Identify the blood parasite species.
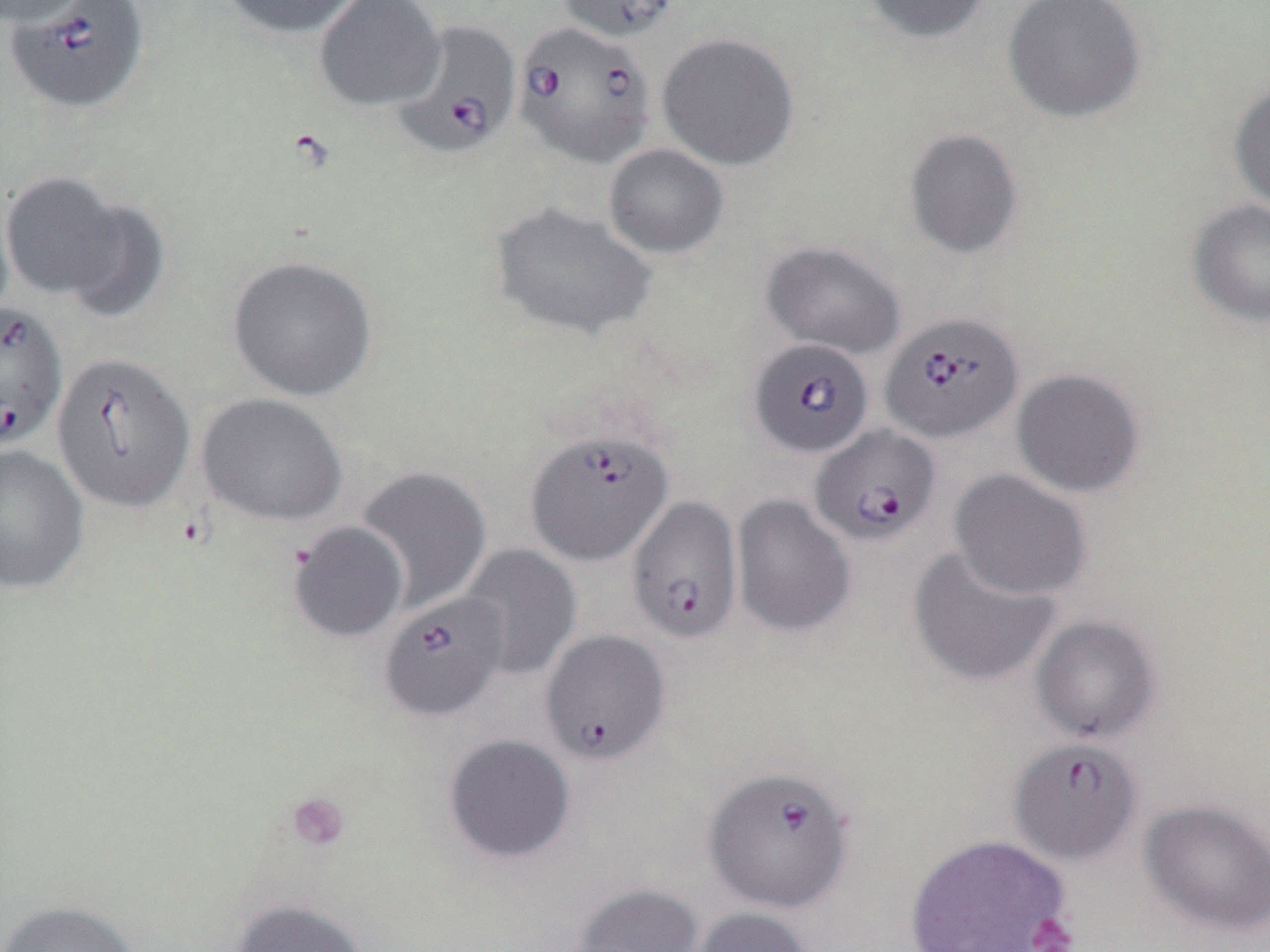
Babesia divergens.

stain = May-Grünwald-Giemsa
image size = 1270×952 pixels
modality = light microscopy
uninfected red blood cell locations = approximate bounding boxes as (x1,y1)-(x2,y2) corner pairs in pixels: (0,0)-(95,28), (214,0)-(366,39), (314,0)-(445,111), (556,0)-(682,42), (860,0)-(992,45), (1003,0)-(1147,124), (656,31)-(800,171), (1228,78)-(1270,214), (903,128)-(1025,260), (603,143)-(730,259), (0,171)-(130,303), (55,194)-(172,324), (1187,198)-(1270,327), (490,202)-(657,341), (760,239)-(905,358), (227,255)-(378,402), (1011,368)-(1145,498), (196,392)-(348,526), (0,444)-(89,595), (354,465)-(492,613), (948,468)-(1093,601), (731,494)-(856,638), (287,521)-(409,643), (458,543)-(582,682), (906,545)-(1062,689), (1030,614)-(1162,744), (442,733)-(576,865), (1138,798)-(1270,936), (903,833)-(1072,952), (565,883)-(704,952), (230,898)-(371,952), (0,899)-(141,952), (683,906)-(816,952)
field of view = one of a larger specimen
preparation = thin blood film
platelet locations = approximate bounding boxes as (x1,y1)-(x2,y2) corner pairs in pixels: (285,791)-(350,852), (1026,913)-(1079,952)
magnification = 1000x
Babesia divergens-infected red blood cell locations = approximate bounding boxes as (x1,y1)-(x2,y2) corner pairs in pixels: (5,1)-(151,114), (393,19)-(521,159), (512,21)-(656,169), (0,299)-(68,450), (880,310)-(1023,444), (748,338)-(874,458), (51,351)-(196,513), (810,424)-(941,546), (525,428)-(674,565), (626,496)-(743,645), (379,592)-(508,722), (539,628)-(671,766), (1009,736)-(1142,865), (702,764)-(855,913)